State which parasite is depicted.
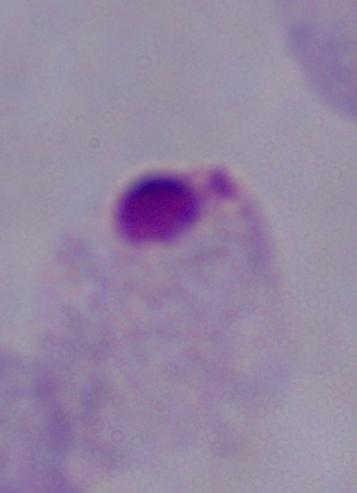

This is a trichomonad.

1000x magnification. Photomicrograph.